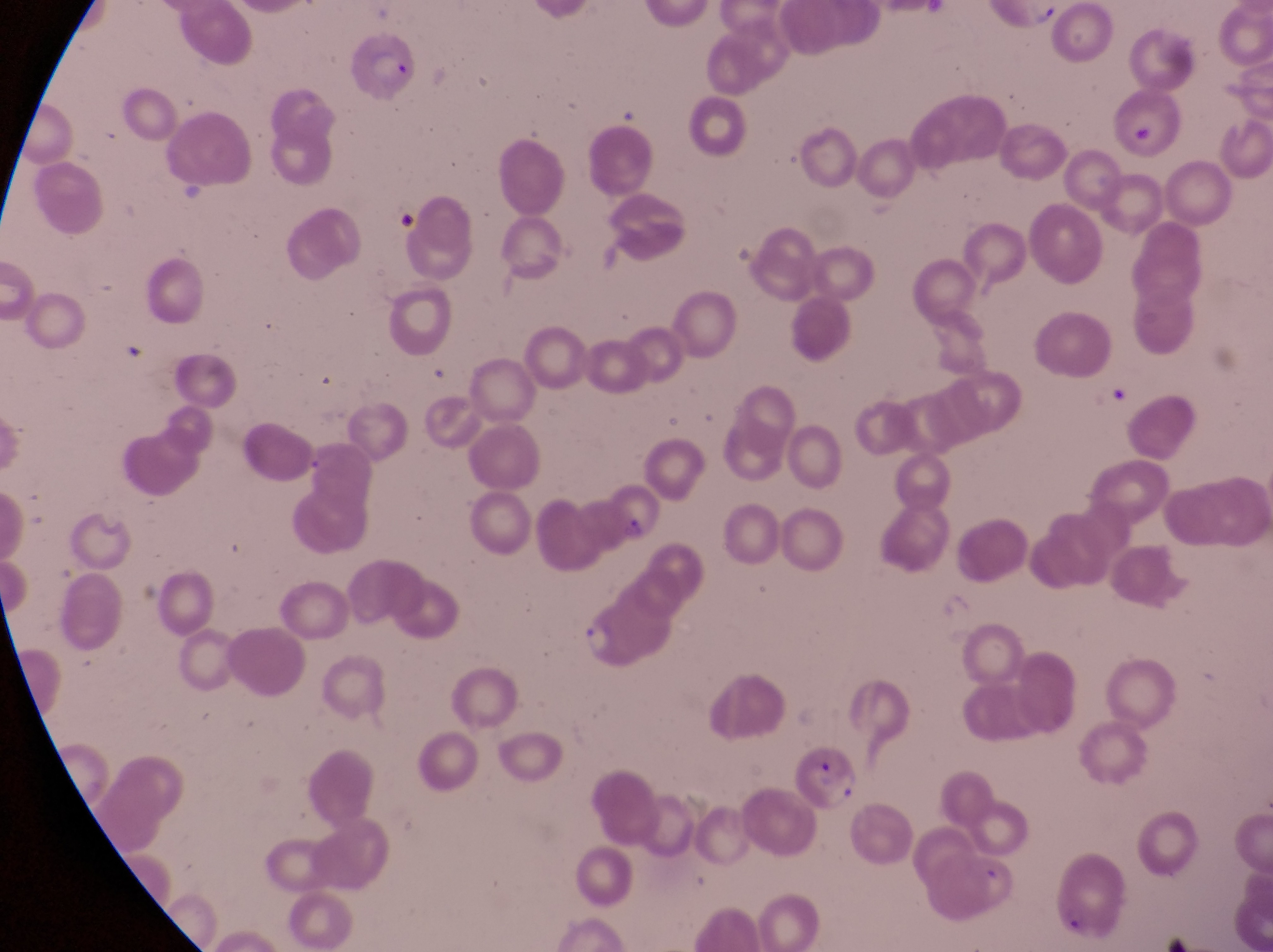
{
  "trophozoite_locations": "approximate bounding boxes as left top right bottom in pixels: 577 619 625 662",
  "parasitised_red_blood_cell_locations": "approximate bounding boxes as left top right bottom in pixels: 352 32 421 109; 596 477 658 537; 796 746 870 813; 1056 862 1133 937",
  "image_size": "1273×952 pixels",
  "preparation": "thin blood film",
  "magnification": "1000x",
  "capture": "smartphone photograph through the eyepiece of an Olympus CX-23 microscope",
  "country": "Uganda",
  "field_of_view": "single"
}